Assess the morphology of the red blood cells.
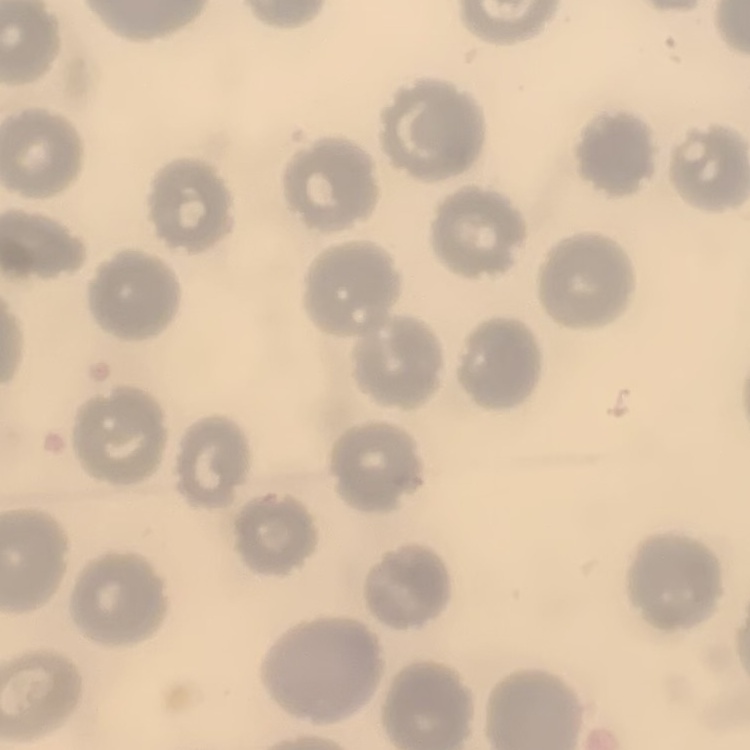

No rouleaux formation.

Summary:
  - Stain: Field's or Giemsa
  - Image type: one tile cut from a larger photomicrograph
  - Preparation: thin blood smear